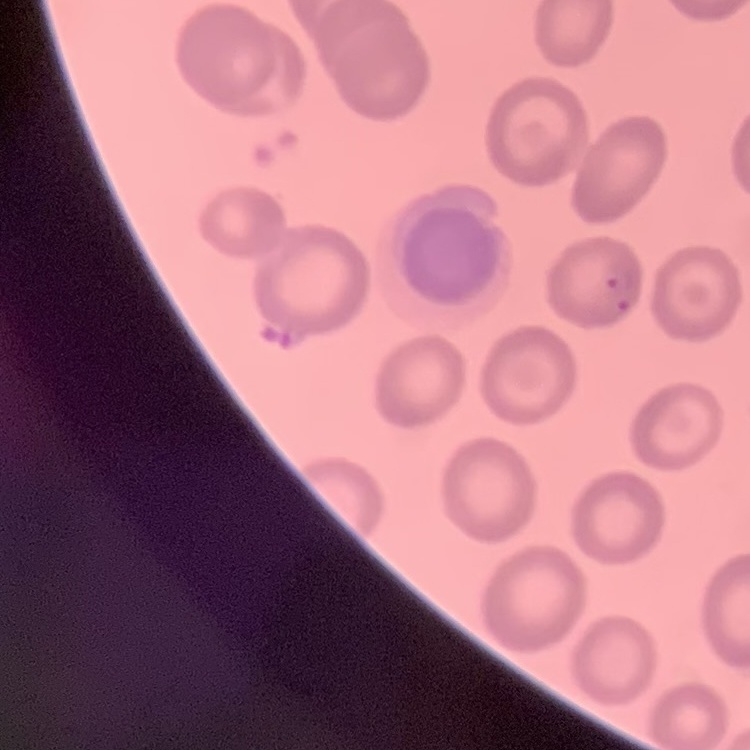
Summary:
  - Erythrocyte morphology: no rouleaux formation
  - Preparation: thin blood smear
  - Image type: square crop of a larger photomicrograph
  - Stain: Field's or Giemsa